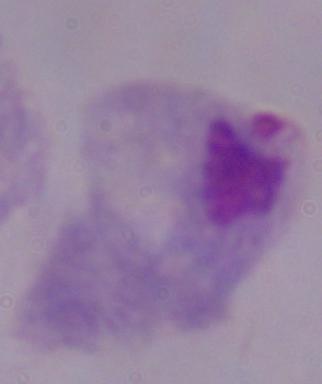

Captured at 1000x magnification. Micrograph. A trichomonad is shown.